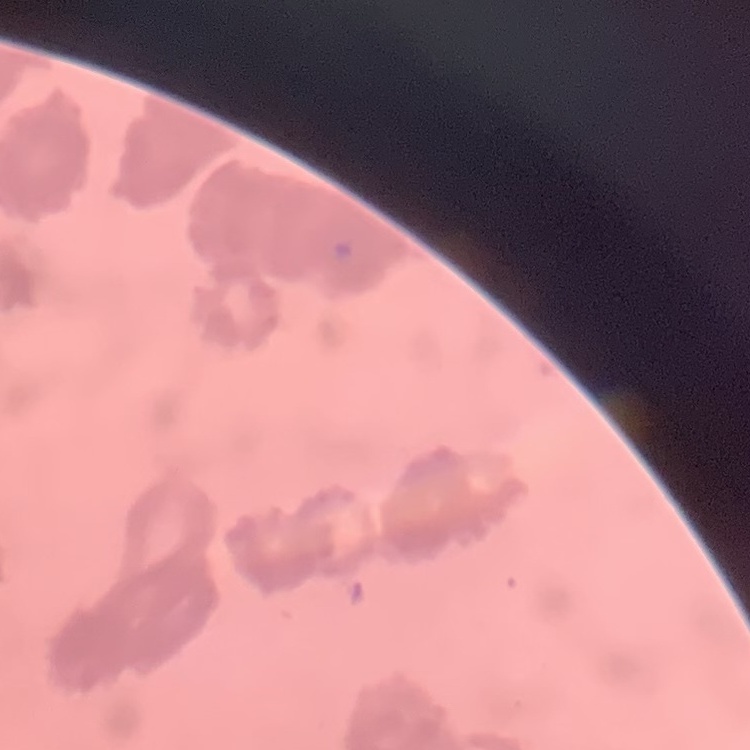

Summary:
  - Red blood cell morphology: rouleaux formation
  - Stain: Field's or Giemsa
  - Image type: square crop of a larger photomicrograph
  - Preparation: thin peripheral smear